Assess this cell for malaria.
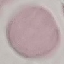
Uninfected.

capture = smartphone camera at the microscope eyepiece
image type = cell patch, automatically extracted from a larger field of view and resized to 64 × 64 pixels
stain = Giemsa
preparation = thin blood smear